Report the malaria status of this cell.
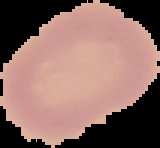
Uninfected.

preparation = thin blood smear
image size = 160×148 pixels
image type = segmented cell region on a black background